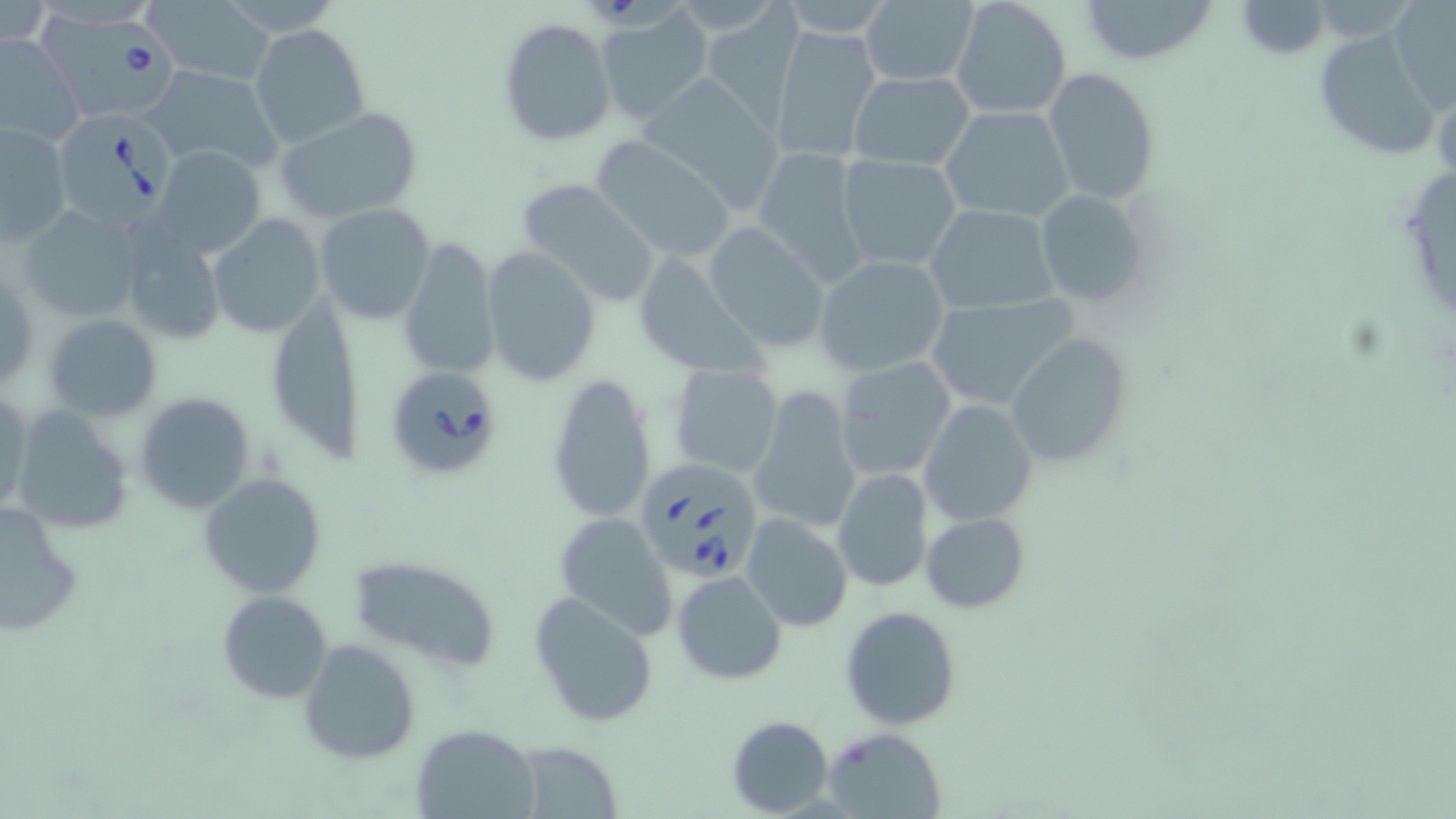

Summary:
  - Coordinate format: approximate bounding boxes as named x1/y1/x2/y2 corners in pixels
  - Babesia divergens-infected red blood cell locations: (x1=32, y1=13, x2=184, y2=124), (x1=50, y1=111, x2=180, y2=229), (x1=382, y1=365, x2=506, y2=483), (x1=636, y1=455, x2=766, y2=585)
  - Uninfected red blood cell locations: (x1=949, y1=0, x2=1072, y2=120), (x1=1079, y1=0, x2=1220, y2=67), (x1=1233, y1=1, x2=1332, y2=58), (x1=1388, y1=1, x2=1456, y2=113), (x1=145, y1=2, x2=277, y2=87), (x1=858, y1=2, x2=979, y2=86), (x1=702, y1=5, x2=803, y2=130), (x1=593, y1=7, x2=712, y2=124), (x1=497, y1=18, x2=615, y2=146), (x1=250, y1=23, x2=371, y2=149), (x1=769, y1=25, x2=882, y2=164), (x1=1312, y1=29, x2=1443, y2=162), (x1=0, y1=31, x2=84, y2=147), (x1=143, y1=65, x2=284, y2=173), (x1=1042, y1=68, x2=1160, y2=206), (x1=849, y1=70, x2=976, y2=171), (x1=640, y1=74, x2=789, y2=217), (x1=939, y1=106, x2=1074, y2=223), (x1=277, y1=107, x2=425, y2=224), (x1=2, y1=120, x2=71, y2=242), (x1=587, y1=136, x2=739, y2=264), (x1=153, y1=145, x2=266, y2=258), (x1=752, y1=146, x2=870, y2=288), (x1=836, y1=154, x2=964, y2=270), (x1=175, y1=158, x2=295, y2=302), (x1=517, y1=178, x2=661, y2=306), (x1=1032, y1=188, x2=1149, y2=307), (x1=313, y1=203, x2=435, y2=325), (x1=923, y1=203, x2=1061, y2=314), (x1=16, y1=204, x2=145, y2=326), (x1=208, y1=214, x2=324, y2=338), (x1=703, y1=223, x2=832, y2=352), (x1=119, y1=231, x2=225, y2=345), (x1=398, y1=239, x2=500, y2=380), (x1=480, y1=246, x2=600, y2=386), (x1=630, y1=249, x2=767, y2=381), (x1=813, y1=255, x2=950, y2=378), (x1=919, y1=295, x2=1080, y2=414), (x1=270, y1=304, x2=363, y2=470), (x1=43, y1=313, x2=162, y2=422), (x1=1006, y1=332, x2=1133, y2=465), (x1=834, y1=357, x2=958, y2=484), (x1=667, y1=364, x2=785, y2=479), (x1=546, y1=372, x2=658, y2=526), (x1=749, y1=385, x2=862, y2=535), (x1=1, y1=387, x2=33, y2=521), (x1=133, y1=392, x2=257, y2=515), (x1=918, y1=399, x2=1037, y2=527), (x1=9, y1=405, x2=136, y2=535), (x1=833, y1=468, x2=933, y2=593), (x1=197, y1=471, x2=328, y2=597), (x1=1, y1=500, x2=85, y2=637), (x1=553, y1=512, x2=678, y2=641), (x1=920, y1=512, x2=1030, y2=613), (x1=742, y1=515, x2=852, y2=632), (x1=348, y1=555, x2=499, y2=672), (x1=673, y1=570, x2=787, y2=685), (x1=214, y1=591, x2=334, y2=703), (x1=530, y1=592, x2=660, y2=729), (x1=841, y1=605, x2=962, y2=731), (x1=242, y1=609, x2=381, y2=748), (x1=298, y1=639, x2=420, y2=766), (x1=726, y1=715, x2=835, y2=816), (x1=412, y1=725, x2=540, y2=817), (x1=823, y1=728, x2=949, y2=819), (x1=513, y1=739, x2=624, y2=817)
  - Slide-level diagnosis: Babesia divergens
  - Modality: light microscopy
  - Image size: 1456×819 pixels
  - Stain: May-Grünwald-Giemsa
  - Field of view: single
  - Preparation: thin blood smear
  - Magnification: 1000x